Classify this cell by malaria status.
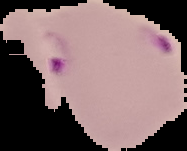
It is parasitized.

Summary:
  - Image type: segmented cell region with the area outside set to black
  - Image size: 187×151 pixels
  - Preparation: thin blood smear